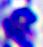
Summary:
  - Modality: micrograph
  - Magnification: 400x
  - Identification: white blood cell